Give the extent of all Plasmodium malariae-infected red blood cells.
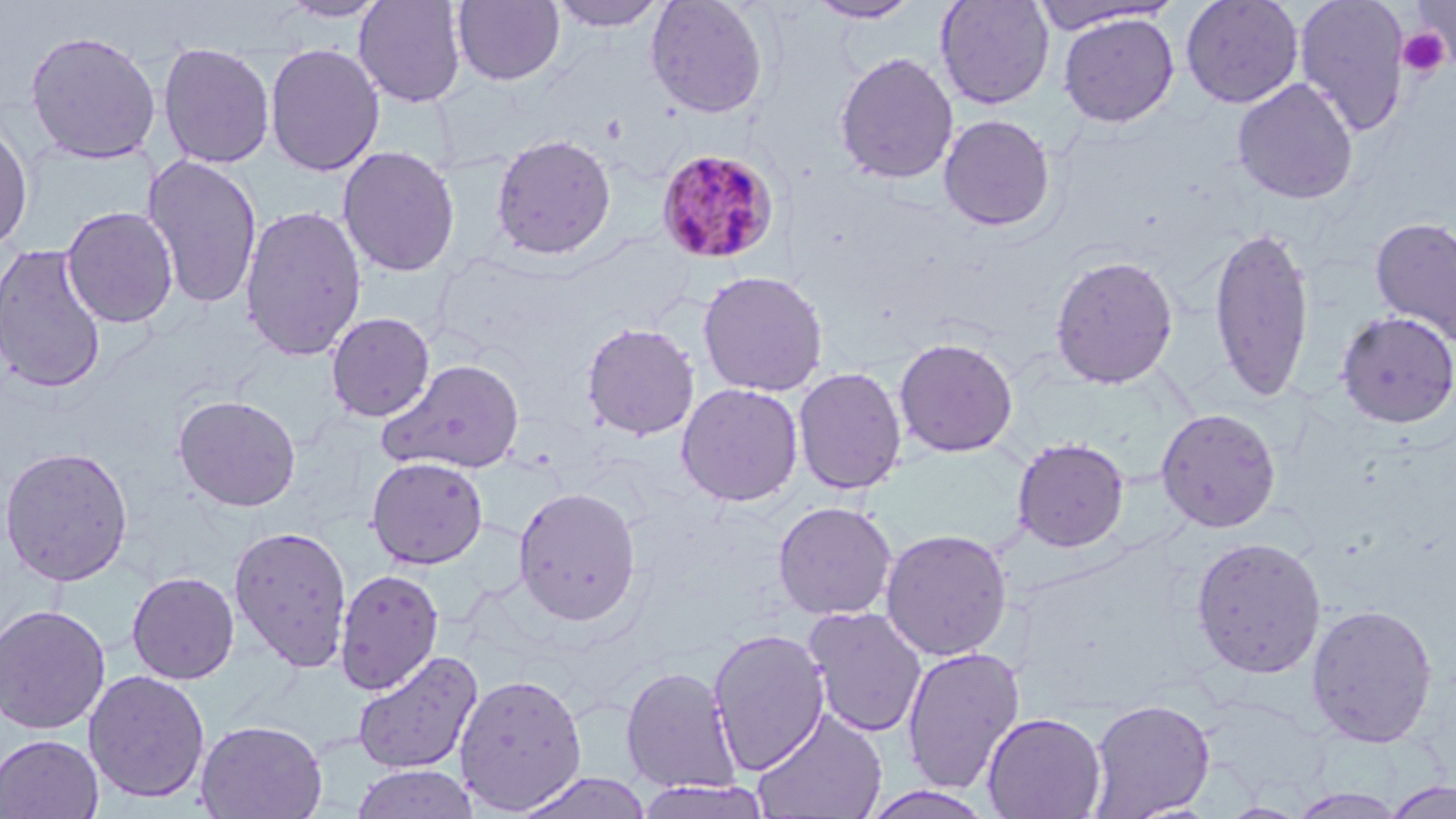
Approximate bounding boxes as (x1,y1)-(x2,y2) corner pairs in pixels.
Plasmodium malariae-infected red blood cells: (655,148)-(780,265).

Summary:
  - Uninfected red blood cell locations: (278,0)-(391,23), (353,0)-(468,108), (452,0)-(565,86), (548,0)-(669,31), (645,0)-(770,119), (1180,0)-(1304,109), (1295,0)-(1410,138), (1408,0)-(1456,67), (806,1)-(921,24), (935,1)-(1056,110), (1029,1)-(1184,34), (1058,12)-(1180,128), (24,29)-(162,164), (157,42)-(275,169), (264,43)-(384,177), (835,51)-(958,185), (1231,78)-(1359,204), (938,114)-(1056,232), (0,117)-(34,255), (491,133)-(617,260), (337,145)-(460,277), (142,154)-(263,311), (239,205)-(366,362), (60,206)-(179,328), (1369,216)-(1456,346), (1207,224)-(1316,402), (0,244)-(108,393), (1048,254)-(1179,389), (697,270)-(829,397), (1335,310)-(1455,429), (325,312)-(435,422), (581,321)-(700,441), (894,336)-(1018,457), (378,358)-(525,474), (793,367)-(907,495), (676,382)-(804,507), (173,394)-(301,511), (1156,407)-(1282,533), (1012,437)-(1130,552), (0,445)-(134,586), (366,456)-(488,569), (513,487)-(641,626), (773,500)-(897,621), (228,524)-(352,673), (880,528)-(1013,661), (1190,535)-(1327,678), (334,568)-(444,694), (126,570)-(240,684), (0,603)-(111,734), (1305,603)-(1439,748), (803,606)-(928,738), (707,628)-(830,775), (900,645)-(1025,795), (351,650)-(483,775), (621,665)-(741,794), (83,669)-(210,803), (453,671)-(587,814), (1196,693)-(1330,802), (1086,699)-(1216,818), (751,708)-(888,819), (982,712)-(1106,819), (195,718)-(328,819), (0,733)-(104,818), (350,764)-(479,819), (515,772)-(653,819), (638,778)-(773,819), (1383,781)-(1456,819), (859,786)-(998,819), (1288,788)-(1409,818)
  - Platelet locations: (1410,3)-(1455,65), (1398,27)-(1451,80)
  - Slide-level diagnosis: Plasmodium malariae
  - Modality: light microscopy
  - Stain: May-Grünwald-Giemsa
  - Magnification: 1000x
  - Preparation: thin blood film
  - Image size: 1456×819 pixels
  - Field of view: single